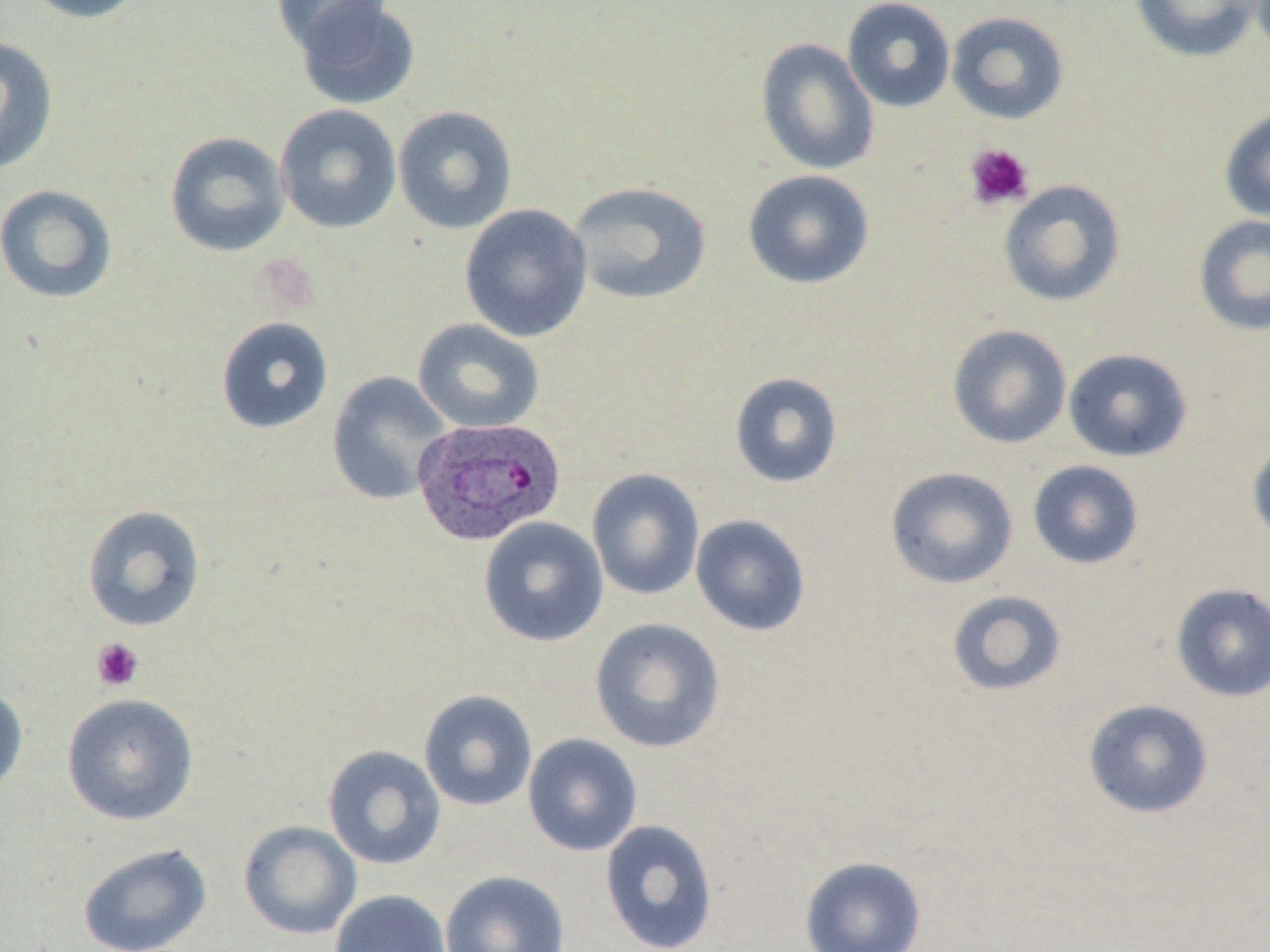

Approximate bounding boxes as [x1, y1, x2, y2] in pixels. Plasmodium ovale-infected red blood cell locations: [412, 417, 567, 546]. Uninfected red blood cell locations: [21, 0, 148, 24], [271, 0, 394, 53], [293, 0, 421, 110], [842, 0, 956, 113], [1131, 0, 1265, 62], [946, 11, 1069, 125], [0, 35, 58, 175], [756, 38, 879, 175], [275, 104, 401, 234], [393, 105, 518, 234], [1219, 107, 1270, 223], [165, 131, 290, 257], [743, 169, 875, 289], [998, 180, 1126, 307], [567, 181, 712, 306], [0, 184, 118, 304], [459, 203, 593, 342], [1193, 214, 1270, 337], [215, 316, 334, 434], [413, 319, 545, 434], [947, 325, 1072, 449], [1063, 348, 1192, 462], [327, 371, 453, 505], [729, 372, 843, 488], [1247, 437, 1270, 546], [1027, 460, 1144, 570], [885, 466, 1018, 589], [587, 468, 705, 601], [82, 504, 206, 632], [690, 514, 811, 636], [478, 517, 608, 647], [1170, 583, 1270, 702], [947, 590, 1067, 697], [590, 617, 726, 754], [0, 684, 29, 802], [418, 690, 538, 811], [61, 692, 198, 825], [1082, 698, 1214, 819], [522, 733, 642, 857], [322, 744, 446, 870], [599, 818, 719, 952], [238, 820, 362, 939], [77, 842, 213, 952], [799, 856, 927, 952], [440, 870, 569, 952], [330, 890, 451, 952]. Platelet locations: [964, 143, 1034, 211], [91, 638, 144, 692]. Slide-level diagnosis: Plasmodium ovale. Thin blood film. May-Grünwald-Giemsa-stained preparation. Light microscopy. Single field of view. Captured at 1000x magnification. Image is 1270×952 pixels.